Outline each uninfected red blood cell.
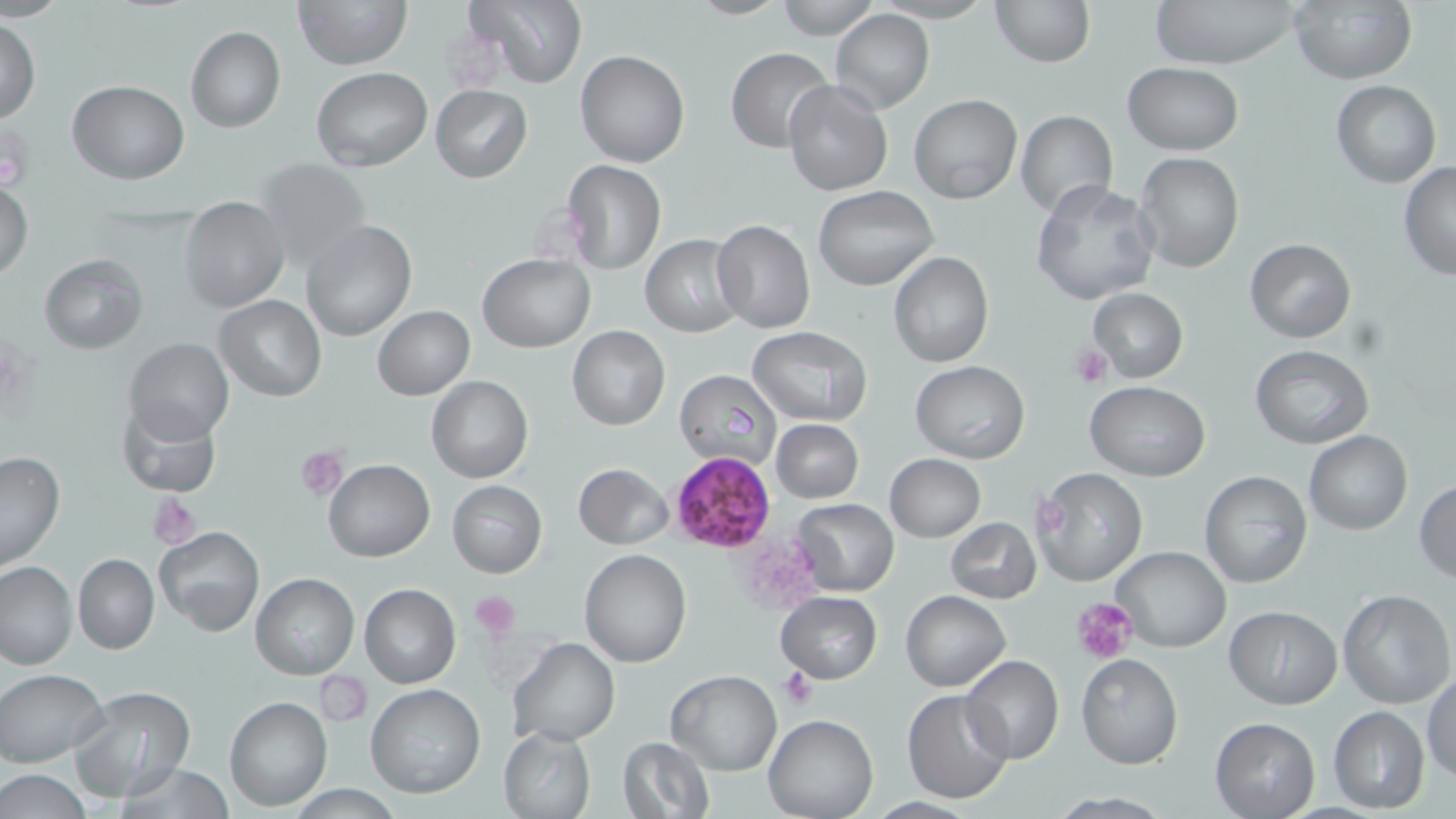

Approximate bounding boxes as named x1/y1/x2/y2 corners in pixels.
Uninfected red blood cells: (x1=293, y1=0, x2=411, y2=70), (x1=461, y1=0, x2=589, y2=90), (x1=775, y1=0, x2=878, y2=38), (x1=991, y1=0, x2=1093, y2=67), (x1=1152, y1=0, x2=1302, y2=69), (x1=1292, y1=0, x2=1416, y2=84), (x1=830, y1=9, x2=933, y2=113), (x1=1, y1=14, x2=40, y2=123), (x1=185, y1=27, x2=286, y2=133), (x1=725, y1=47, x2=834, y2=152), (x1=576, y1=51, x2=689, y2=168), (x1=1122, y1=62, x2=1244, y2=155), (x1=314, y1=68, x2=432, y2=170), (x1=67, y1=80, x2=190, y2=183), (x1=784, y1=80, x2=892, y2=196), (x1=1331, y1=80, x2=1441, y2=187), (x1=430, y1=85, x2=532, y2=183), (x1=909, y1=94, x2=1023, y2=204), (x1=1015, y1=109, x2=1118, y2=220), (x1=1134, y1=152, x2=1245, y2=274), (x1=254, y1=157, x2=373, y2=272), (x1=560, y1=160, x2=666, y2=275), (x1=1398, y1=163, x2=1456, y2=281), (x1=1, y1=177, x2=33, y2=283), (x1=1030, y1=179, x2=1159, y2=305), (x1=814, y1=186, x2=939, y2=292), (x1=178, y1=198, x2=290, y2=314), (x1=300, y1=220, x2=417, y2=340), (x1=712, y1=220, x2=816, y2=334), (x1=642, y1=235, x2=745, y2=338), (x1=1244, y1=239, x2=1356, y2=343), (x1=888, y1=251, x2=994, y2=367), (x1=480, y1=253, x2=595, y2=352), (x1=39, y1=254, x2=147, y2=354), (x1=1088, y1=289, x2=1187, y2=382), (x1=214, y1=294, x2=326, y2=401), (x1=373, y1=306, x2=474, y2=400), (x1=568, y1=324, x2=670, y2=430), (x1=746, y1=326, x2=873, y2=425), (x1=125, y1=338, x2=234, y2=445), (x1=1251, y1=344, x2=1374, y2=449), (x1=910, y1=360, x2=1031, y2=463), (x1=676, y1=368, x2=781, y2=474), (x1=426, y1=376, x2=532, y2=483), (x1=1085, y1=381, x2=1208, y2=481), (x1=116, y1=399, x2=221, y2=495), (x1=771, y1=418, x2=863, y2=503), (x1=1305, y1=431, x2=1412, y2=535), (x1=0, y1=449, x2=65, y2=572), (x1=883, y1=454, x2=984, y2=541), (x1=323, y1=459, x2=434, y2=562), (x1=573, y1=463, x2=674, y2=550), (x1=1032, y1=467, x2=1147, y2=587), (x1=1199, y1=470, x2=1314, y2=590), (x1=446, y1=480, x2=547, y2=578), (x1=1414, y1=480, x2=1456, y2=582), (x1=794, y1=499, x2=899, y2=596), (x1=946, y1=516, x2=1041, y2=603), (x1=154, y1=525, x2=264, y2=636), (x1=1113, y1=546, x2=1230, y2=653), (x1=578, y1=547, x2=693, y2=668), (x1=72, y1=552, x2=159, y2=655), (x1=0, y1=560, x2=77, y2=668), (x1=250, y1=573, x2=358, y2=679), (x1=359, y1=583, x2=461, y2=687), (x1=776, y1=590, x2=882, y2=683), (x1=900, y1=590, x2=1011, y2=692), (x1=1337, y1=590, x2=1454, y2=710), (x1=1225, y1=605, x2=1341, y2=709), (x1=506, y1=637, x2=620, y2=746), (x1=1077, y1=654, x2=1184, y2=769), (x1=960, y1=655, x2=1065, y2=766), (x1=0, y1=668, x2=109, y2=768), (x1=665, y1=671, x2=783, y2=775), (x1=1424, y1=671, x2=1455, y2=781), (x1=367, y1=684, x2=486, y2=799), (x1=69, y1=686, x2=196, y2=802), (x1=903, y1=690, x2=1014, y2=803), (x1=224, y1=695, x2=332, y2=809), (x1=1328, y1=706, x2=1429, y2=813), (x1=764, y1=714, x2=879, y2=819), (x1=1209, y1=716, x2=1319, y2=818), (x1=500, y1=725, x2=596, y2=817), (x1=616, y1=737, x2=715, y2=819), (x1=115, y1=763, x2=235, y2=818), (x1=0, y1=769, x2=94, y2=817).

slide_level_diagnosis: Plasmodium falciparum
stain: May-Grünwald-Giemsa
field_of_view: one of a larger specimen
plasmodium_falciparum_infected_red_blood_cell_locations: 'approximate bounding boxes as named x1/y1/x2/y2 corners in pixels: (x1=669, y1=452, x2=774, y2=552)'
image_size: 1456×819 pixels
magnification: 1000x
modality: light microscopy
preparation: thin blood film
platelet_locations: 'approximate bounding boxes as named x1/y1/x2/y2 corners in pixels: (x1=1, y1=127, x2=35, y2=191), (x1=1069, y1=342, x2=1113, y2=388), (x1=296, y1=445, x2=347, y2=499), (x1=147, y1=492, x2=203, y2=549), (x1=471, y1=590, x2=523, y2=638), (x1=1071, y1=596, x2=1136, y2=665), (x1=776, y1=666, x2=818, y2=708)'